Report the malaria status of this cell.
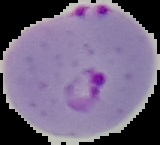
It is parasitized.

image_size: 160×145 pixels
preparation: thin blood smear
image_type: segmented cell region with the area outside set to black